Point out each malaria parasite.
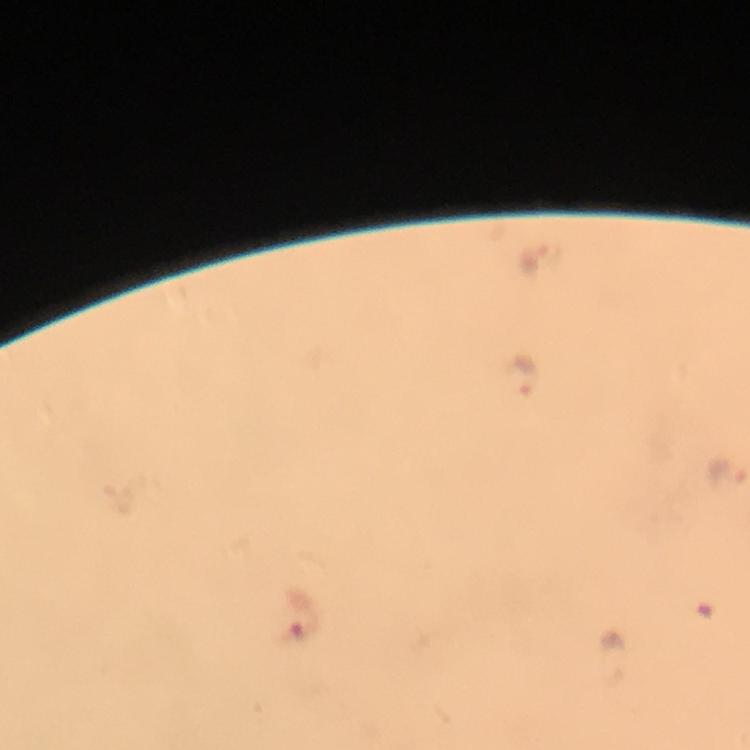
Approximate centers as {x, y} in pixels.
Malaria parasites: {534, 264}, {524, 374}, {722, 470}.

Thick blood smear. A crop from one field of view. Immersion oil was used. At 100x magnification. Image is 750×750 pixels. Photographed through the microscope with a smartphone camera. From a malaria diagnostic workup. Giemsa-stained preparation.